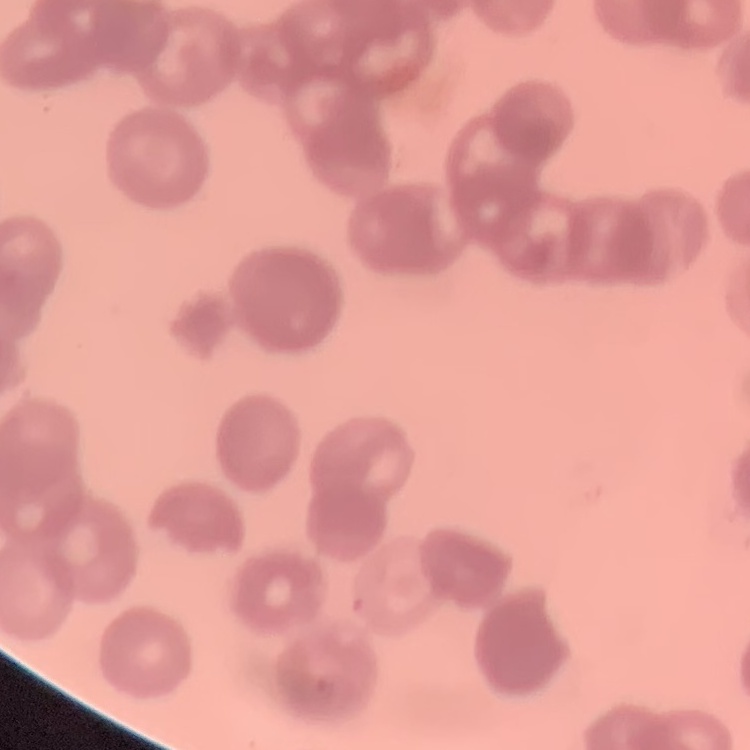

Summary:
  - Erythrocyte morphology: rouleaux formation
  - Image type: square crop of a larger photomicrograph
  - Preparation: thin blood film
  - Stain: Field's or Giemsa